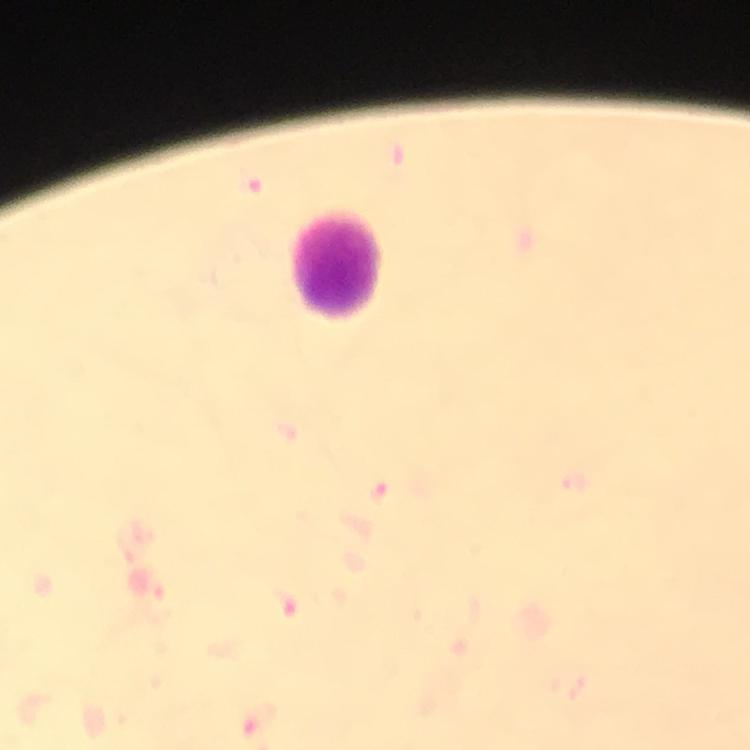
immersion_oil: applied
magnification: 100x
preparation: thick blood film
plasmodium_parasite_locations: 'approximate centers as {x, y} in pixels: {256, 183}, {379, 492}'
context: from a malaria diagnostic workup
stain: Giemsa
leukocyte_locations: 'approximate centers as {x, y} in pixels: {339, 269}'
image_size: 750×750 pixels
cropped_from: a single field of view
capture: smartphone camera through the microscope